State which parasite is depicted.
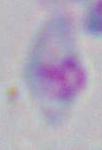
Toxoplasma gondii.

Micrograph. 1000x magnification.